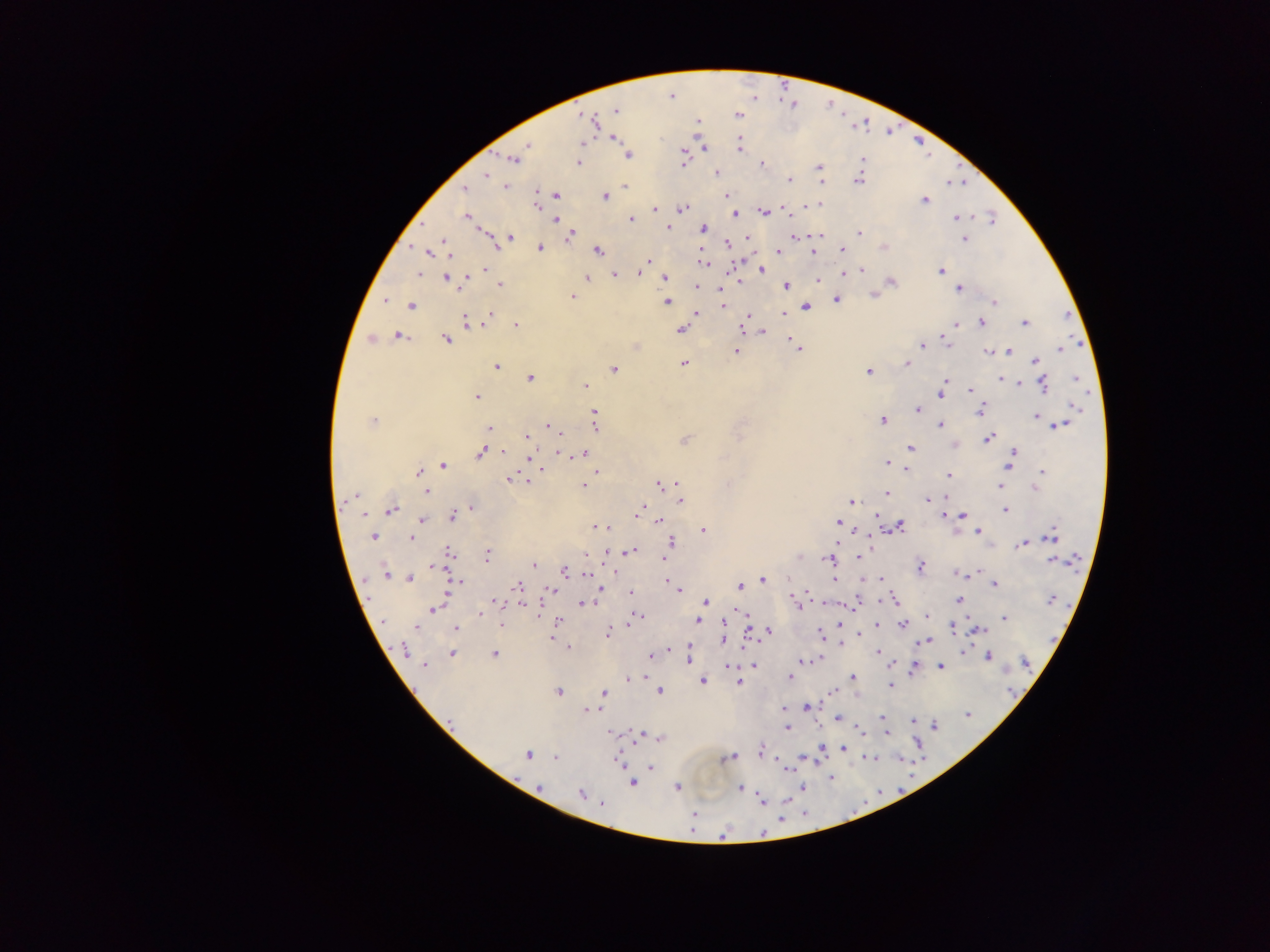

Approximate centers as (x, y) in pixels.
Summary:
  - Malaria parasite locations: (671, 96), (615, 110), (737, 114), (586, 118), (697, 122), (592, 123), (614, 137), (582, 142), (527, 144), (739, 144), (703, 148), (628, 155), (512, 159), (683, 160), (579, 163), (761, 164), (819, 168), (716, 172), (486, 175), (789, 179), (858, 180), (820, 182), (625, 185), (464, 187), (505, 187), (724, 192), (555, 193), (537, 194), (727, 194), (604, 195), (923, 200), (820, 203), (536, 204), (808, 204), (655, 209), (682, 209), (784, 209), (763, 211), (735, 214), (467, 216), (956, 217), (555, 219), (630, 219), (992, 220), (667, 227), (701, 228), (860, 232), (820, 235), (746, 236), (510, 237), (569, 237), (794, 237), (964, 239), (496, 242), (727, 243), (884, 247), (540, 248), (813, 250), (842, 250), (430, 251), (598, 251), (777, 251), (647, 259), (703, 262), (484, 269), (861, 269), (761, 270), (940, 270), (848, 271), (416, 273), (639, 273), (614, 274), (447, 277), (664, 278), (586, 279), (817, 279), (465, 280), (738, 280), (891, 281), (500, 284), (695, 286), (721, 286), (785, 286), (958, 288), (873, 295), (573, 296), (385, 300), (836, 300), (667, 301), (994, 303), (411, 305), (723, 305), (806, 306), (695, 313), (782, 313), (491, 314), (748, 315), (488, 318), (465, 321), (1023, 322), (982, 323), (956, 324), (516, 325), (680, 329), (743, 330), (763, 331), (397, 335), (788, 335), (371, 338), (446, 339), (943, 339), (792, 340), (923, 343), (636, 346), (798, 349), (1060, 349), (1010, 350), (737, 351), (988, 352), (1035, 361), (683, 363), (906, 363), (496, 367), (614, 369), (868, 370), (529, 377), (1074, 378), (1000, 379), (946, 381), (1020, 384), (1044, 384), (584, 386), (969, 391), (940, 393), (477, 396), (1074, 408), (918, 410), (980, 410), (594, 412), (1035, 417), (882, 419), (374, 421), (940, 424), (595, 425), (1058, 425), (548, 426), (488, 429), (526, 437), (988, 437), (683, 440), (954, 446), (910, 448), (505, 451), (1014, 451), (560, 452), (482, 453), (582, 454), (1009, 460), (886, 464), (442, 465), (542, 469), (906, 469), (1043, 471), (418, 472), (597, 472), (948, 476), (508, 479), (527, 480), (676, 483), (660, 485), (583, 486), (999, 486), (1035, 488), (425, 492), (886, 493), (680, 500), (927, 501), (852, 502), (472, 508), (390, 509), (640, 509), (1005, 510), (364, 514), (877, 515), (944, 515), (963, 515), (452, 516), (422, 520), (656, 520), (837, 522), (899, 525), (597, 526), (607, 526), (703, 529), (979, 530), (871, 533), (374, 536), (1051, 537), (411, 538), (671, 542), (836, 542), (1022, 544), (630, 551), (450, 553), (486, 554), (585, 555), (797, 556), (663, 558), (858, 558), (827, 559), (1052, 559), (434, 565), (534, 565), (920, 567), (563, 571), (978, 573), (586, 574), (961, 574), (384, 575), (410, 577), (762, 579), (880, 579), (835, 580), (456, 581), (666, 581), (994, 583), (740, 585), (518, 586), (678, 590), (550, 591), (630, 591), (598, 592), (807, 594), (793, 599), (1051, 599), (958, 600), (496, 601), (894, 601), (705, 602), (821, 602), (583, 603), (798, 603), (521, 604), (853, 606), (436, 607), (480, 614), (745, 615), (639, 616), (926, 616), (634, 618), (1004, 618), (558, 619), (697, 620), (629, 622), (502, 623), (838, 623), (877, 624), (903, 624), (416, 626), (951, 628), (456, 630), (980, 630), (767, 631), (747, 633), (607, 634), (820, 634), (858, 634), (551, 639), (724, 640), (927, 641), (839, 643), (567, 646), (402, 649), (689, 651), (963, 651), (877, 652), (452, 653), (495, 654), (989, 655), (650, 656), (820, 658), (688, 660), (799, 662), (892, 664), (425, 665), (727, 665), (754, 665), (940, 666), (914, 668), (646, 677), (789, 677), (627, 678), (851, 678), (702, 681), (739, 682), (890, 685), (658, 691), (557, 692), (832, 692), (604, 693), (806, 708), (595, 709), (783, 709), (584, 710), (966, 715), (882, 717), (837, 718), (913, 721), (934, 726), (787, 727), (860, 730), (611, 733), (886, 733), (639, 735), (658, 738), (843, 748), (821, 749), (759, 752), (528, 755), (555, 757), (729, 757), (872, 757), (898, 757), (802, 758), (617, 759), (650, 767), (785, 768), (831, 778), (632, 782), (803, 786), (539, 787), (677, 787), (741, 788), (581, 793), (760, 801), (602, 804), (693, 814)
  - Capture: mobile-phone photograph through a microscope
  - Image size: 1270×952 pixels
  - Field of view: single
  - Country: Ghana
  - Preparation: thick blood film